Locate every Plasmodium falciparum-infected red blood cell.
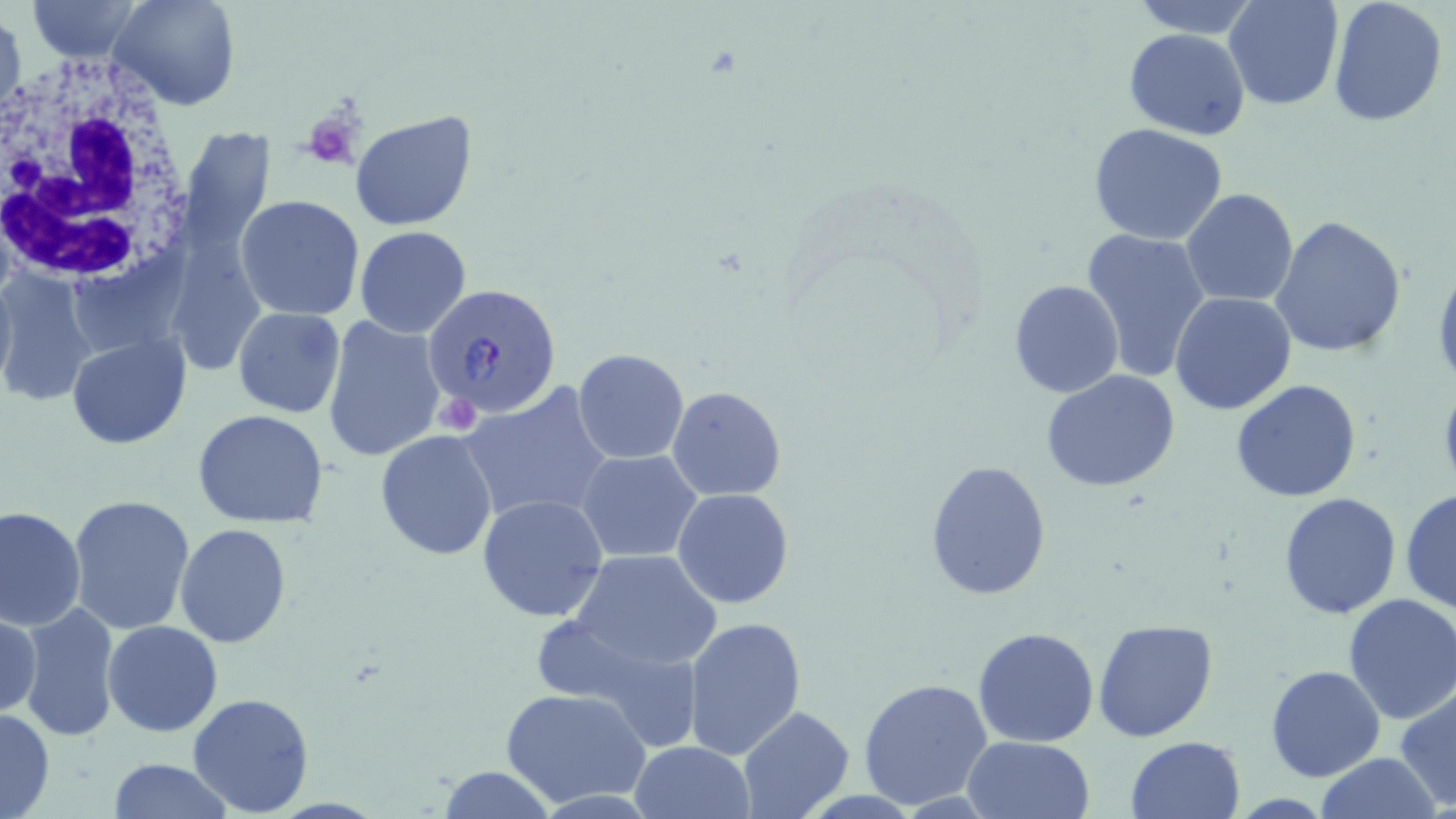
Approximate bounding boxes as named x1/y1/x2/y2 corners in pixels.
Plasmodium falciparum-infected red blood cells: (x1=425, y1=284, x2=563, y2=418).

Platelet locations: (x1=302, y1=111, x2=359, y2=169). Uninfected red blood cell locations: (x1=26, y1=0, x2=142, y2=62), (x1=109, y1=0, x2=241, y2=112), (x1=1125, y1=0, x2=1262, y2=38), (x1=1223, y1=0, x2=1343, y2=110), (x1=1328, y1=0, x2=1449, y2=126), (x1=1, y1=12, x2=24, y2=123), (x1=1122, y1=28, x2=1250, y2=140), (x1=351, y1=108, x2=479, y2=231), (x1=1087, y1=123, x2=1230, y2=245), (x1=180, y1=126, x2=273, y2=262), (x1=1180, y1=188, x2=1299, y2=308), (x1=235, y1=194, x2=365, y2=320), (x1=1272, y1=216, x2=1408, y2=358), (x1=354, y1=225, x2=472, y2=338), (x1=1081, y1=226, x2=1212, y2=382), (x1=1038, y1=236, x2=1189, y2=445), (x1=1432, y1=260, x2=1456, y2=395), (x1=0, y1=265, x2=16, y2=395), (x1=0, y1=272, x2=99, y2=407), (x1=1008, y1=279, x2=1125, y2=400), (x1=1169, y1=292, x2=1297, y2=414), (x1=233, y1=306, x2=345, y2=418), (x1=321, y1=316, x2=448, y2=464), (x1=67, y1=334, x2=191, y2=450), (x1=572, y1=348, x2=689, y2=463), (x1=1042, y1=372, x2=1182, y2=493), (x1=1231, y1=377, x2=1363, y2=502), (x1=1437, y1=378, x2=1456, y2=497), (x1=459, y1=382, x2=613, y2=526), (x1=667, y1=385, x2=786, y2=501), (x1=192, y1=409, x2=331, y2=530), (x1=375, y1=429, x2=499, y2=561), (x1=578, y1=449, x2=702, y2=562), (x1=924, y1=458, x2=1052, y2=600), (x1=577, y1=471, x2=794, y2=593), (x1=1401, y1=486, x2=1456, y2=615), (x1=673, y1=489, x2=795, y2=607), (x1=1278, y1=492, x2=1402, y2=619), (x1=68, y1=493, x2=197, y2=635), (x1=477, y1=494, x2=610, y2=624), (x1=1, y1=506, x2=86, y2=630), (x1=175, y1=523, x2=291, y2=649), (x1=565, y1=550, x2=721, y2=673), (x1=1342, y1=593, x2=1456, y2=724), (x1=17, y1=601, x2=122, y2=742), (x1=1, y1=609, x2=41, y2=723), (x1=683, y1=615, x2=806, y2=762), (x1=1094, y1=618, x2=1218, y2=740), (x1=102, y1=620, x2=225, y2=737), (x1=973, y1=626, x2=1100, y2=748), (x1=1266, y1=665, x2=1386, y2=782), (x1=858, y1=676, x2=993, y2=809), (x1=1395, y1=684, x2=1456, y2=811), (x1=501, y1=688, x2=651, y2=808), (x1=186, y1=691, x2=314, y2=816), (x1=737, y1=704, x2=854, y2=818), (x1=0, y1=705, x2=54, y2=819), (x1=1125, y1=735, x2=1245, y2=818), (x1=963, y1=736, x2=1096, y2=819), (x1=629, y1=741, x2=756, y2=819), (x1=1313, y1=754, x2=1446, y2=818), (x1=107, y1=758, x2=231, y2=818), (x1=436, y1=765, x2=554, y2=819). White blood cell locations: (x1=0, y1=53, x2=202, y2=290). Slide-level diagnosis: Plasmodium falciparum. Captured at 1000x magnification. Thin blood film. May-Grünwald-Giemsa-stained preparation. Optical microscopy. One field of a larger specimen. Image is 1456×819 pixels.